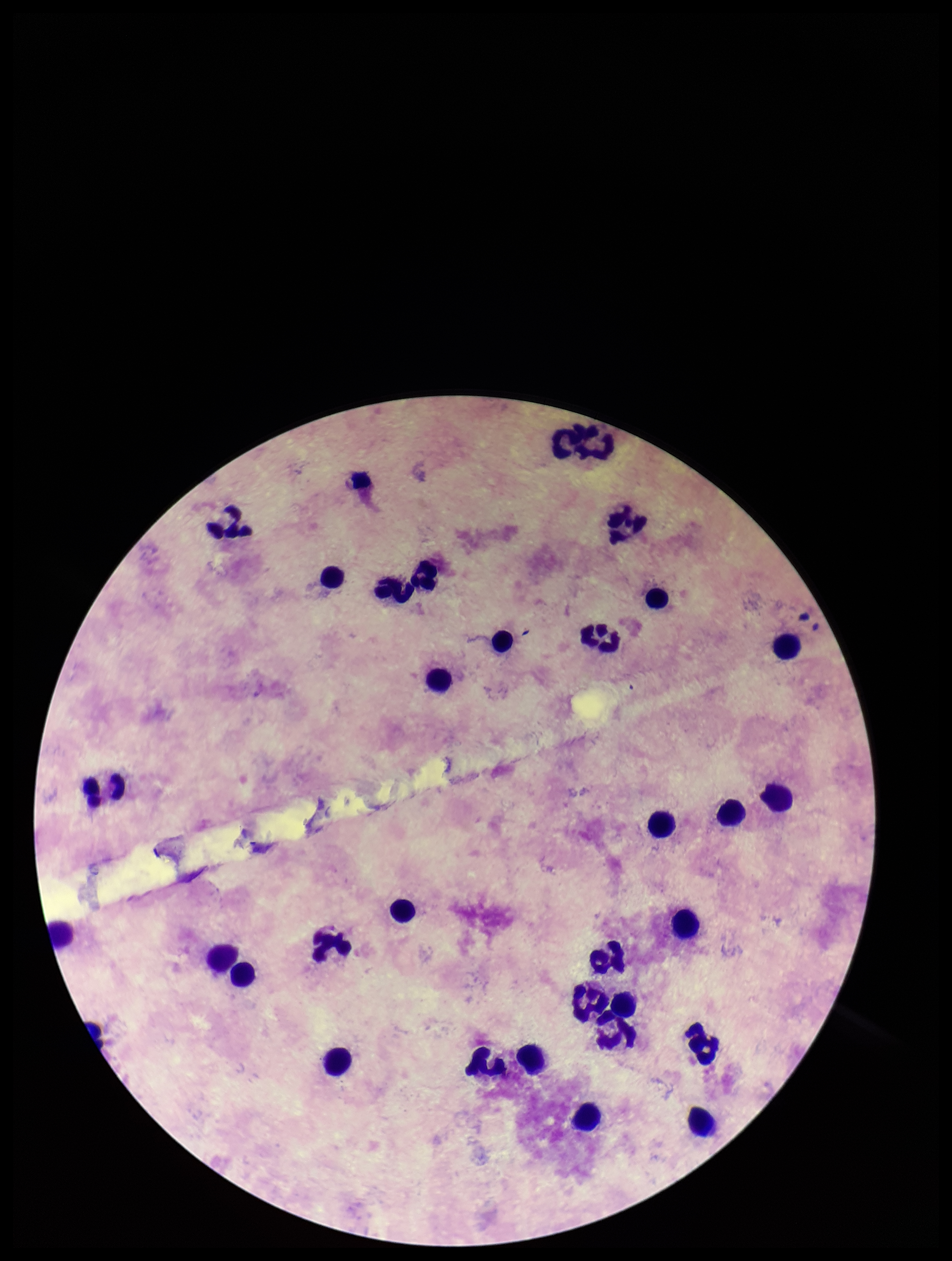

Summary:
  - Image size: 952×1261 pixels
  - Parasite count: 0
  - Field of view: single
  - Leukocyte count: 34
  - Preparation: thick smear
  - Patient malaria status: negative
  - Stain: Giemsa
  - Capture: smartphone photograph through the microscope eyepiece
  - Plasmodium parasites: none detected